Classify this cell by malaria status.
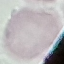
Uninfected.

Giemsa stain. Thin blood smear. Acquired by smartphone through the microscope eyepiece. Automatically extracted cell patch, resized to 64 × 64 pixels.